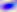 Micrograph. Toxoplasma gondii is seen. Captured at 400x magnification.